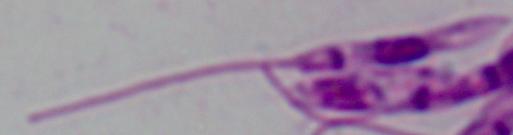
Summary:
  - Modality: micrograph
  - Identification: Leishmania
  - Magnification: 1000x